Outline each uninfected red blood cell.
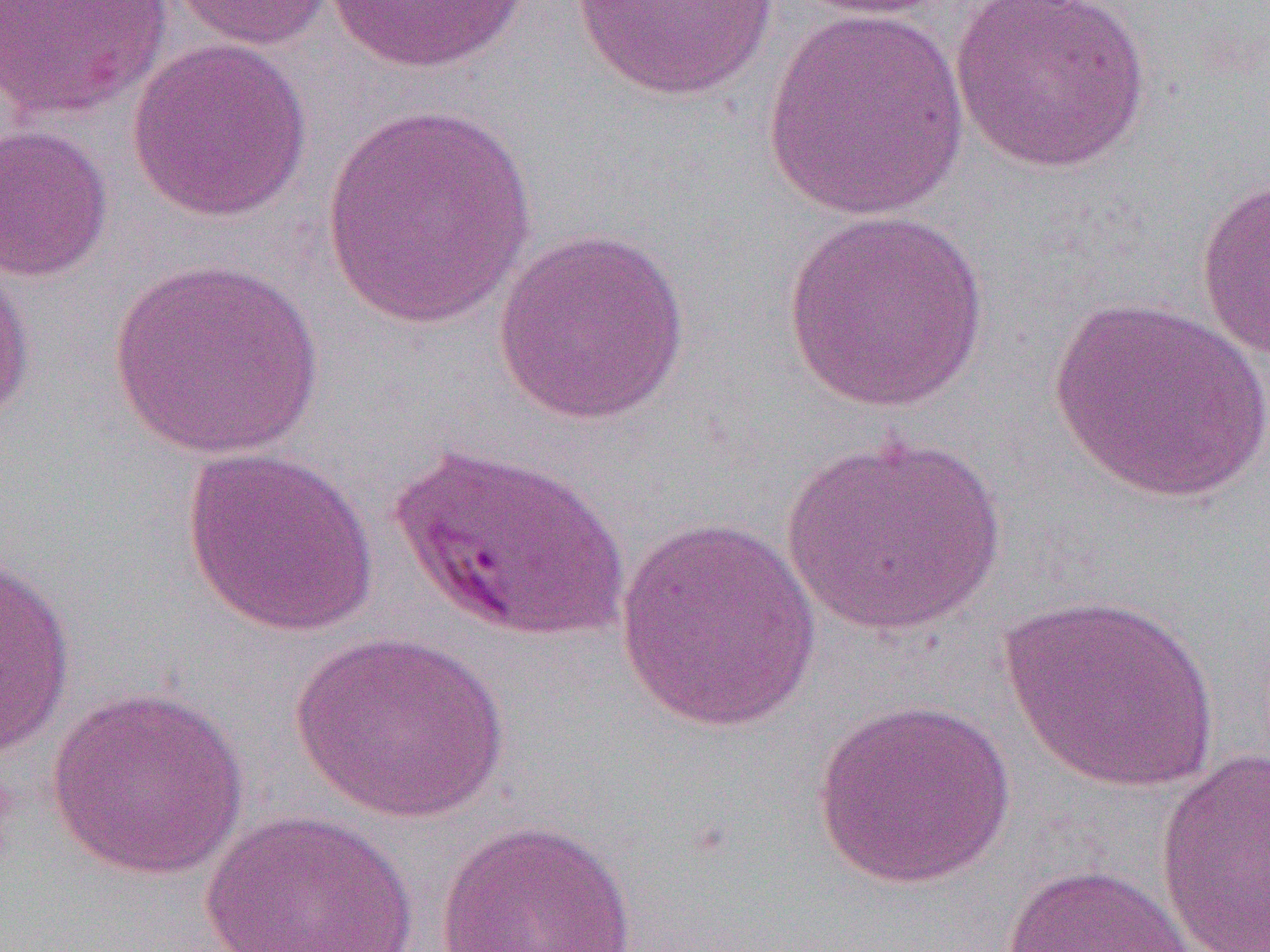
Approximate bounding boxes as [x1, y1, x2, y2] in pixels.
Uninfected red blood cells: [0, 0, 173, 122], [165, 0, 337, 51], [564, 0, 790, 104], [782, 0, 957, 20], [950, 0, 1153, 175], [321, 1, 533, 74], [761, 6, 972, 222], [126, 38, 314, 224], [320, 105, 539, 330], [0, 123, 114, 283], [1195, 176, 1270, 366], [780, 209, 990, 414], [491, 226, 693, 424], [0, 253, 38, 427], [107, 259, 326, 460], [1048, 296, 1269, 504], [779, 433, 1008, 637], [180, 446, 380, 639], [615, 517, 824, 735], [0, 551, 77, 760], [998, 592, 1221, 796], [289, 630, 511, 823], [46, 687, 249, 881], [811, 696, 1017, 891], [1154, 748, 1270, 951], [199, 809, 420, 952], [433, 818, 639, 952], [1001, 861, 1199, 952].

Slide-level diagnosis: Plasmodium falciparum. Thin blood smear. Single field of view. Light microscopy. Captured at 1000x magnification. Image is 1270×952 pixels.